Report the malaria status of this cell.
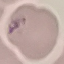

Parasitized.

Acquired by smartphone through the microscope eyepiece. Cell patch, automatically extracted from a larger field of view and resized to 64 × 64 pixels. Thin blood film. Giemsa stain.